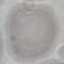

Summary:
  - Result: negative for malaria parasites
  - Capture: smartphone through the microscope eyepiece
  - Image type: cell patch, automatically extracted from a larger field of view and resized to 64 × 64 pixels
  - Preparation: thin smear
  - Stain: Giemsa